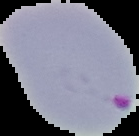 Malaria status: parasitized. Cell region segmented out of the field of view; the surrounding area is masked to black. From a thin blood film. Image is 139×136 pixels.